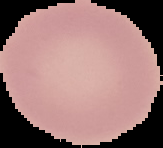

The area outside the segmented cell region is set to black. Image is 163×148 pixels. Malaria status: uninfected. From a thin blood film.